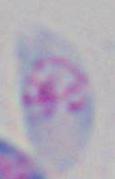
Summary:
  - Magnification: 1000x
  - Modality: micrograph
  - Identification: Toxoplasma gondii